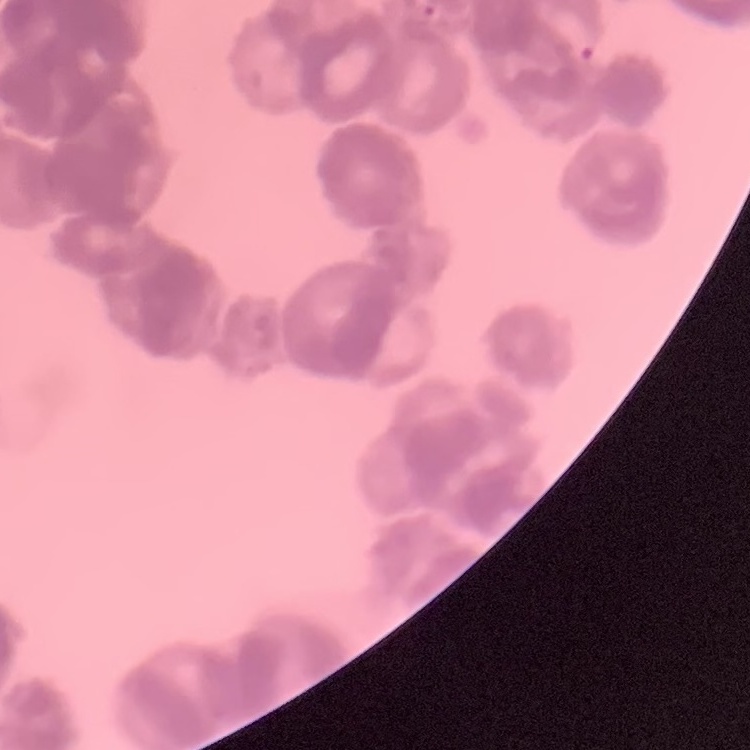
red blood cell morphology = rouleaux formation
stain = Field's or Giemsa
preparation = thin blood film
image type = square crop of a larger photomicrograph